Classify this cell by malaria status.
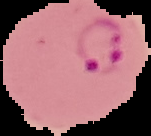

Parasitized.

{
  "image_type": "segmented cell region on a black background",
  "preparation": "thin blood smear",
  "image_size": "151×136 pixels"
}